Assess this cell for malaria.
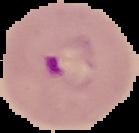

It is parasitized.

preparation = thin blood smear
image type = segmented cell region on a black background
image size = 139×133 pixels